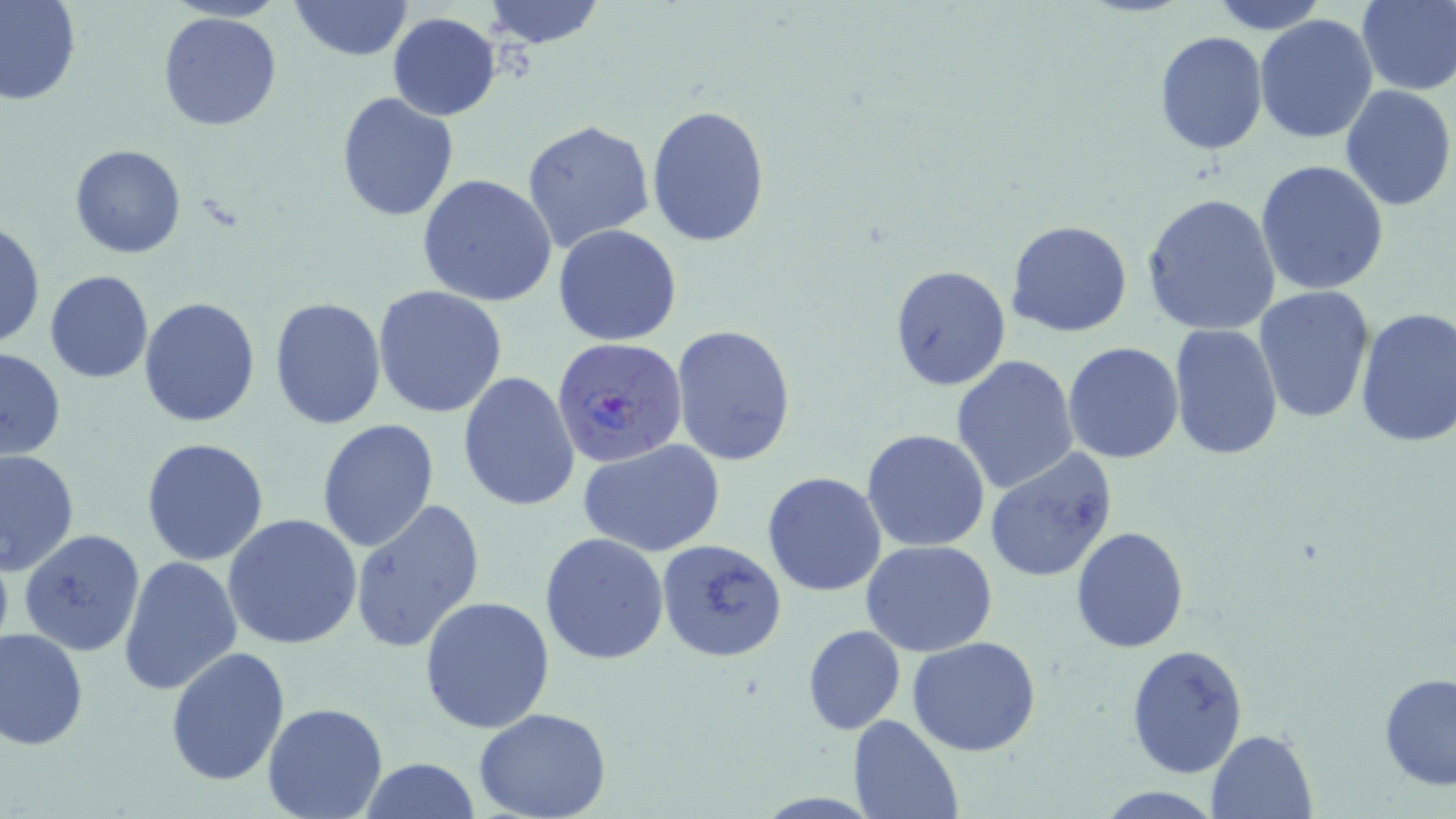

Approximate bounding boxes as (x1,y1)-(x2,y2) corner pairs in pixels. Uninfected red blood cell locations: (0,0)-(82,105), (287,0)-(414,62), (482,0)-(605,48), (1210,0)-(1328,34), (1357,0)-(1456,94), (157,10)-(282,132), (387,13)-(501,120), (1255,13)-(1379,143), (1154,29)-(1268,155), (1339,84)-(1455,212), (335,91)-(460,224), (646,103)-(771,247), (521,119)-(655,251), (69,143)-(188,259), (1255,159)-(1390,297), (416,173)-(558,306), (1141,193)-(1283,337), (1006,220)-(1133,337), (0,221)-(44,351), (553,224)-(682,346), (888,264)-(1011,393), (44,269)-(153,384), (372,285)-(508,418), (1254,286)-(1375,425), (139,296)-(262,429), (269,296)-(386,432), (1354,306)-(1456,447), (670,322)-(798,467), (1170,324)-(1285,460), (1062,340)-(1184,464), (1,345)-(67,460), (950,355)-(1080,494), (458,371)-(580,511), (317,418)-(440,552), (862,428)-(991,552), (140,438)-(270,567), (579,438)-(726,558), (983,447)-(1117,583), (0,449)-(79,576), (761,472)-(887,595), (351,499)-(482,653), (223,514)-(365,651), (1069,525)-(1189,654), (17,528)-(147,658), (540,531)-(670,665), (655,537)-(788,665), (862,539)-(999,656), (119,554)-(243,697), (419,595)-(555,735), (802,624)-(906,736), (0,628)-(87,750), (907,635)-(1041,756), (1125,642)-(1250,779), (164,645)-(290,785), (1379,671)-(1456,790), (262,701)-(389,819), (473,709)-(612,819), (848,715)-(963,819), (1207,729)-(1316,817), (360,757)-(480,818), (1093,787)-(1223,818). Plasmodium falciparum-infected red blood cell locations: (552,335)-(688,471). Slide-level diagnosis: Plasmodium falciparum. Optical microscopy. Captured at 1000x magnification. Single field of view. Image is 1456×819 pixels. Thin blood smear. May-Grünwald-Giemsa stain.